Give the extent of all uninfected red blood cells.
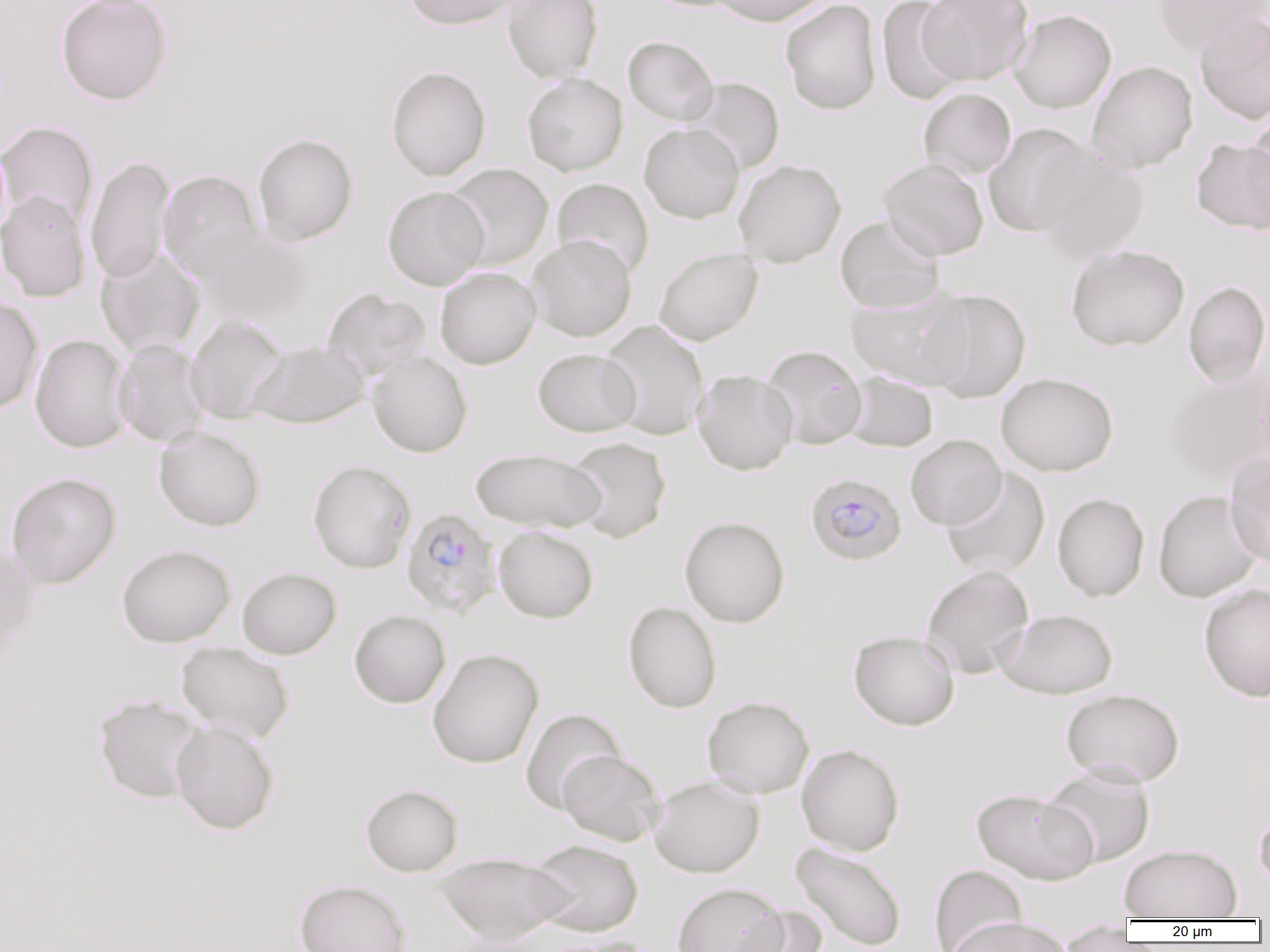
Approximate bounding boxes as [x1, y1, x2, y2] in pixels.
Uninfected red blood cells: [55, 0, 173, 105], [402, 0, 521, 30], [502, 0, 603, 82], [711, 0, 830, 26], [780, 0, 882, 115], [876, 0, 968, 105], [918, 0, 1033, 84], [1152, 0, 1269, 55], [1009, 10, 1116, 113], [1194, 11, 1270, 125], [623, 36, 719, 125], [1087, 60, 1198, 173], [386, 66, 491, 181], [522, 73, 627, 176], [684, 77, 785, 175], [918, 88, 1016, 180], [1246, 111, 1270, 226], [0, 121, 98, 230], [639, 123, 744, 223], [983, 124, 1093, 237], [252, 133, 358, 245], [1191, 139, 1270, 234], [1033, 146, 1150, 261], [85, 155, 175, 284], [878, 158, 989, 260], [733, 159, 846, 267], [444, 163, 553, 271], [158, 170, 263, 279], [551, 178, 654, 279], [382, 186, 489, 290], [0, 190, 90, 302], [835, 215, 946, 313], [194, 224, 313, 325], [526, 234, 637, 341], [1065, 245, 1189, 352], [95, 248, 206, 357], [653, 248, 763, 346], [435, 267, 541, 369], [1183, 280, 1270, 387], [322, 288, 431, 380], [846, 288, 972, 390], [920, 289, 1031, 403], [0, 297, 44, 413], [185, 315, 289, 424], [598, 320, 710, 441], [30, 334, 132, 453], [113, 339, 211, 447], [247, 340, 369, 429], [761, 345, 867, 450], [533, 348, 640, 436], [367, 352, 472, 457], [1252, 359, 1270, 470], [692, 369, 798, 475], [842, 371, 938, 452], [996, 372, 1118, 476], [1164, 374, 1269, 484], [153, 426, 266, 531], [905, 434, 1006, 530], [565, 437, 671, 543], [470, 448, 607, 533], [1224, 453, 1270, 566], [307, 460, 416, 573], [941, 468, 1049, 579], [5, 472, 121, 589], [1153, 490, 1264, 602], [1052, 493, 1149, 601], [679, 516, 790, 627], [493, 526, 598, 623], [0, 544, 41, 654], [117, 544, 235, 647], [921, 565, 1034, 679], [237, 567, 342, 659], [1198, 583, 1270, 701], [623, 601, 722, 713], [996, 609, 1119, 698], [349, 610, 451, 708], [848, 629, 960, 731], [176, 642, 294, 744], [427, 647, 544, 768], [1061, 688, 1185, 786], [92, 693, 206, 804], [702, 696, 814, 798], [520, 708, 626, 814], [170, 720, 279, 835], [796, 744, 905, 855], [557, 750, 664, 845], [1041, 765, 1156, 866], [649, 775, 764, 877], [360, 783, 463, 876], [972, 788, 1099, 885], [1254, 809, 1270, 895], [527, 839, 644, 937], [790, 842, 907, 951], [1119, 843, 1243, 921], [433, 852, 572, 943], [929, 863, 1028, 951], [294, 879, 412, 952], [671, 882, 787, 952], [732, 905, 828, 952], [944, 917, 1073, 952], [1057, 921, 1134, 951], [431, 932, 559, 952], [533, 935, 653, 952].

Plasmodium falciparum-infected red blood cell locations: [805, 472, 906, 566], [401, 508, 501, 618]. Slide-level diagnosis: Plasmodium falciparum. One field of a larger specimen. Light microscopy. Image is 1270×952 pixels. 1000x magnification. Thin blood film.